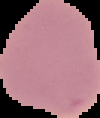

Image is 100×118 pixels. Result: negative for malaria parasites. From a thin blood smear. The area outside the segmented cell region is set to black.